Locate every Plasmodium parasite.
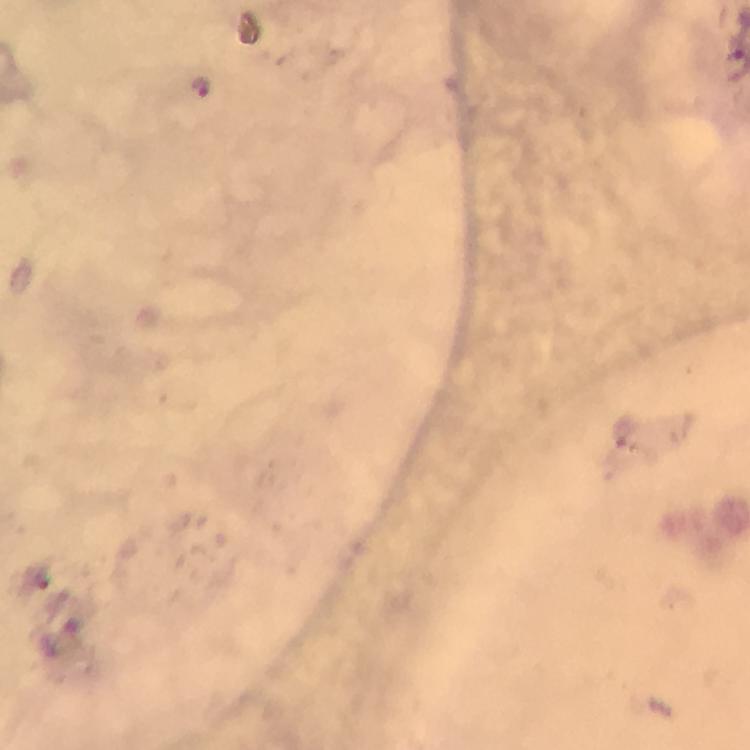
Approximate centers as {x, y} in pixels.
Plasmodium parasites: {201, 87}.

Immersion oil was used. From a diagnostic examination for malaria. Thick smear. Smartphone photograph taken through a microscope. A crop from one field of view. 100x magnification. Image is 750×750 pixels. Giemsa stain.